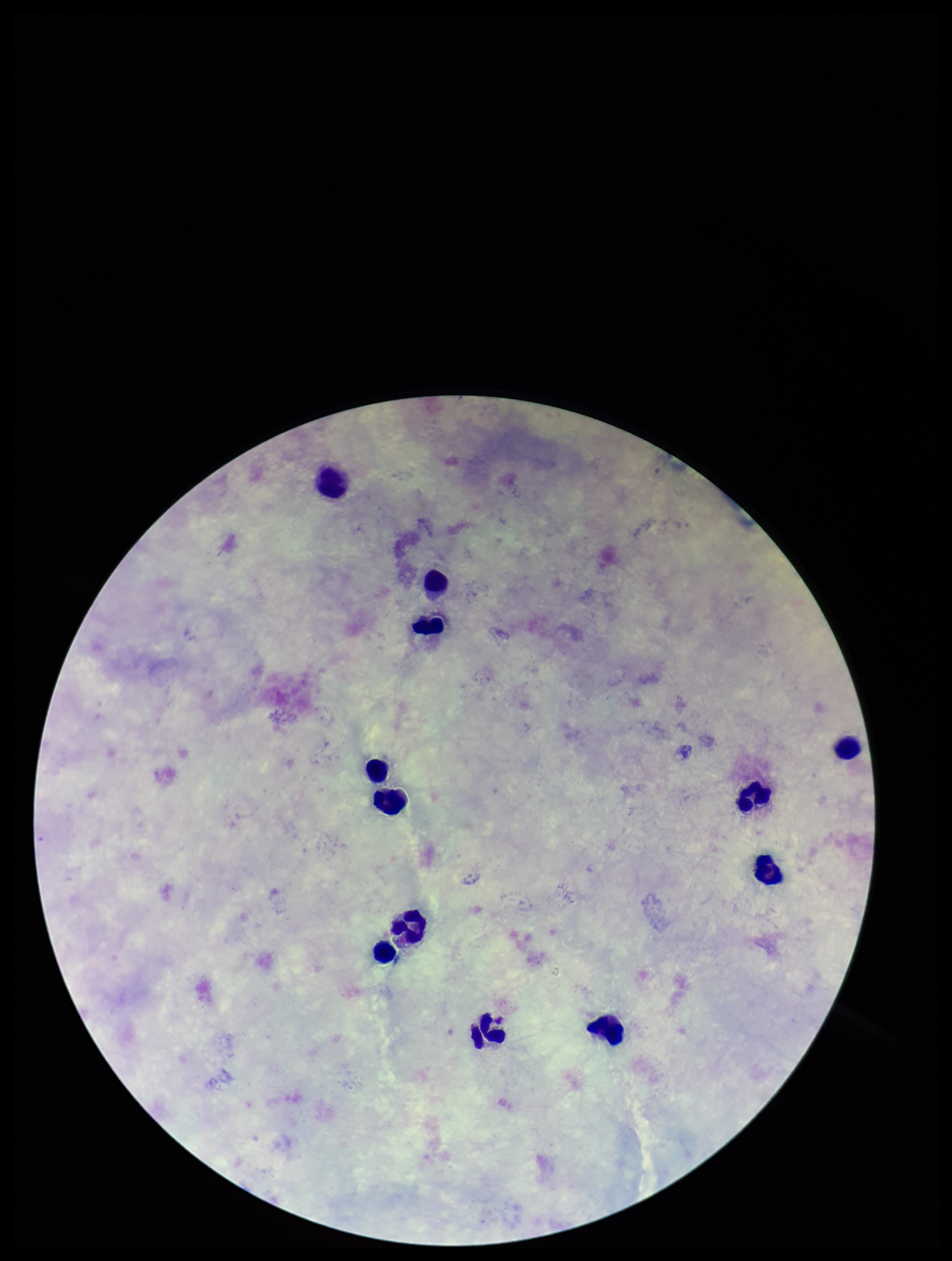

plasmodium_parasites: none detected
patient_malaria_status: negative
image_size: 952×1261 pixels
parasite_count: 0
preparation: thick
field_of_view: single
stain: Giemsa
leukocyte_count: 12
capture: smartphone photograph through the microscope eyepiece